Assess the morphology of the red blood cells.
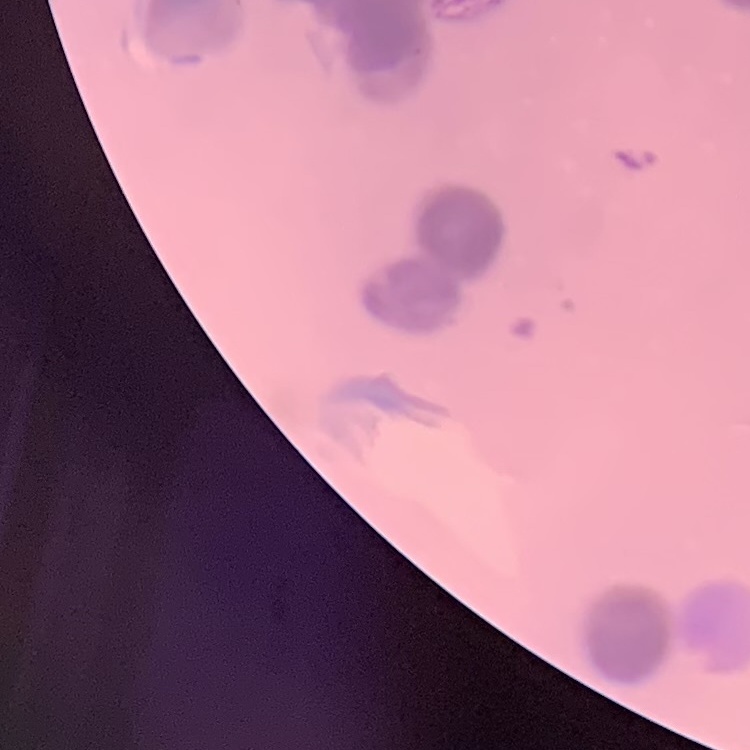

Rouleaux formation.

One tile cut from a larger photomicrograph. Field's or Giemsa stain. Thin blood smear.